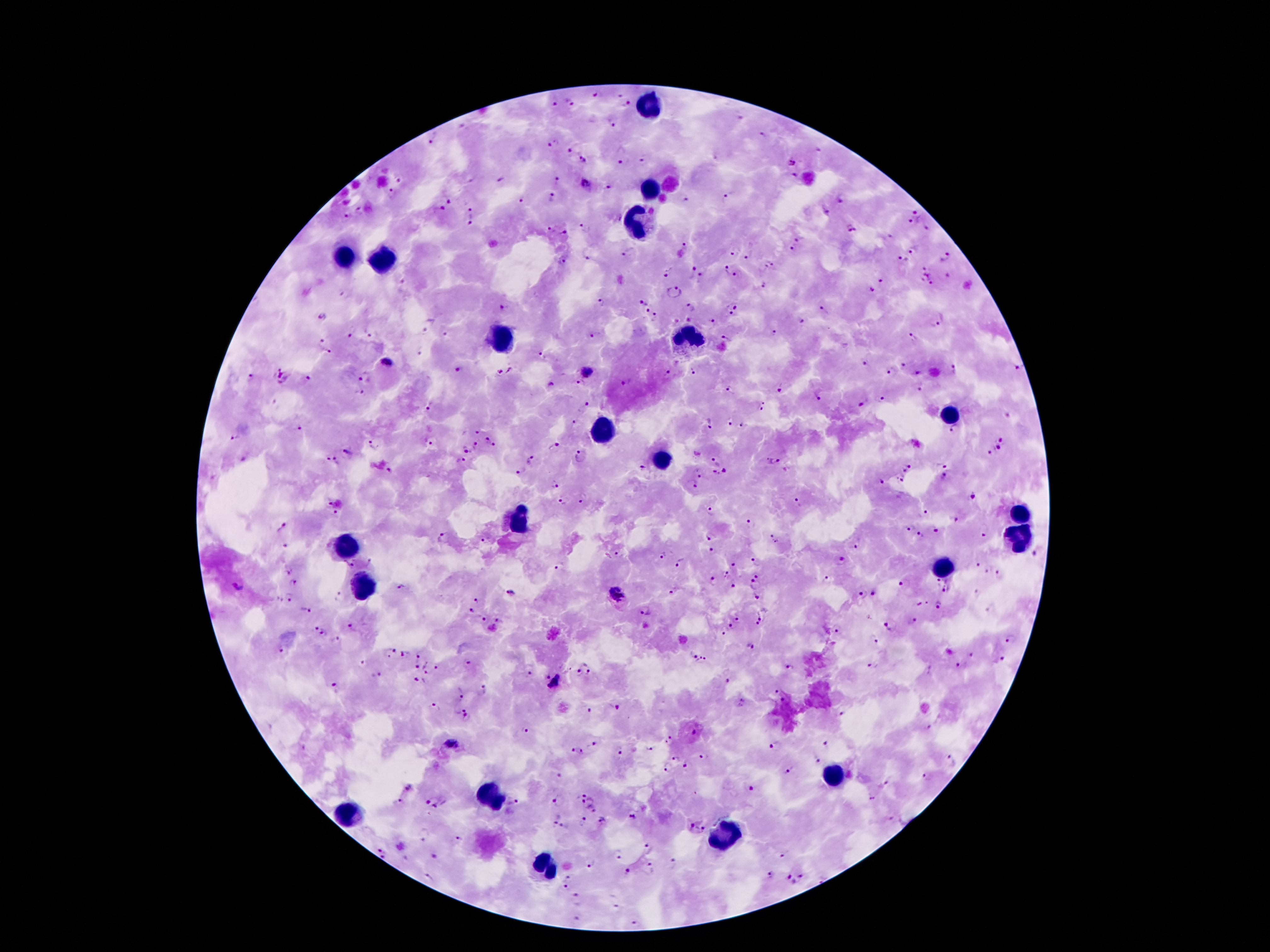
Approximate centers as (x, y) in pixels. Leukocyte locations: (649, 102), (650, 188), (637, 221), (346, 259), (380, 261), (686, 332), (500, 336), (947, 416), (602, 430), (657, 459), (1016, 511), (519, 520), (1018, 541), (348, 547), (941, 566), (364, 586), (830, 775), (489, 797), (346, 814), (725, 836), (546, 866). Malaria parasite locations: (594, 96), (619, 96), (571, 102), (554, 104), (627, 105), (611, 121), (463, 127), (763, 136), (431, 141), (553, 142), (569, 149), (585, 161), (644, 161), (620, 162), (791, 162), (794, 175), (557, 179), (400, 180), (500, 180), (586, 185), (606, 186), (392, 190), (553, 196), (448, 197), (727, 197), (843, 198), (520, 199), (688, 199), (441, 208), (360, 209), (469, 209), (827, 211), (916, 212), (913, 221), (469, 223), (587, 227), (549, 229), (852, 229), (927, 230), (565, 232), (799, 239), (685, 242), (791, 249), (912, 251), (630, 253), (731, 254), (749, 257), (947, 257), (589, 259), (902, 259), (562, 261), (773, 264), (766, 266), (926, 268), (692, 270), (725, 272), (668, 273), (737, 275), (702, 276), (927, 277), (402, 282), (881, 282), (765, 285), (933, 285), (871, 289), (672, 291), (343, 294), (600, 301), (643, 303), (737, 305), (693, 307), (823, 309), (646, 311), (729, 313), (321, 316), (656, 317), (713, 322), (803, 322), (936, 323), (425, 329), (352, 330), (774, 332), (445, 333), (370, 334), (594, 335), (913, 335), (724, 338), (320, 341), (329, 350), (419, 352), (541, 354), (387, 361), (864, 364), (905, 365), (459, 369), (694, 369), (954, 369), (1017, 369), (510, 371), (587, 372), (668, 372), (919, 372), (889, 374), (249, 375), (365, 375), (282, 376), (307, 378), (577, 382), (622, 383), (551, 384), (781, 388), (731, 390), (921, 390), (360, 393), (817, 395), (881, 398), (864, 402), (429, 406), (584, 406), (761, 407), (575, 421), (710, 423), (729, 423), (297, 425), (742, 425), (954, 430), (476, 431), (234, 436), (488, 438), (1003, 438), (431, 441), (916, 443), (474, 444), (494, 444), (373, 445), (554, 447), (465, 448), (997, 449), (346, 452), (989, 453), (578, 456), (329, 459), (715, 459), (462, 460), (531, 460), (774, 460), (337, 461), (942, 464), (644, 467), (909, 467), (389, 470), (521, 470), (725, 470), (904, 471), (716, 474), (944, 475), (699, 476), (882, 480), (899, 480), (554, 483), (690, 485), (972, 496), (582, 497), (560, 502), (329, 503), (799, 503), (711, 509), (927, 512), (336, 513), (956, 518), (750, 522), (282, 528), (908, 529), (936, 531), (920, 535), (710, 536), (442, 537), (774, 537), (984, 537), (482, 539), (858, 543), (286, 544), (712, 549), (615, 555), (1035, 556), (843, 558), (369, 559), (756, 559), (681, 562), (350, 563), (558, 565), (733, 565), (979, 565), (287, 571), (986, 571), (996, 572), (757, 573), (727, 574), (713, 580), (830, 580), (937, 581), (292, 583), (755, 583), (904, 583), (401, 585), (733, 586), (674, 590), (946, 590), (510, 592), (874, 592), (617, 593), (862, 593), (289, 596), (338, 596), (757, 597), (476, 599), (922, 603), (937, 605), (308, 610), (471, 610), (646, 610), (764, 615), (737, 618), (483, 620), (913, 620), (498, 621), (756, 624), (351, 625), (730, 625), (888, 627), (314, 628), (837, 630), (323, 632), (722, 634), (874, 638), (1012, 638), (337, 639), (749, 645), (282, 650), (390, 651), (404, 653), (420, 655), (693, 656), (972, 656), (1003, 659), (702, 660), (360, 662), (469, 663), (874, 665), (416, 666), (425, 666), (958, 666), (436, 667), (789, 667), (427, 671), (578, 671), (588, 672), (529, 674), (378, 675), (548, 676), (416, 679), (726, 680), (556, 682), (335, 687), (485, 690), (775, 691), (462, 693), (783, 700), (435, 706), (618, 707), (461, 708), (591, 710), (843, 714), (467, 719), (929, 726), (523, 731), (693, 732), (670, 740), (594, 742), (827, 743), (451, 744), (776, 745), (572, 748), (651, 748), (582, 751), (618, 753), (702, 755), (676, 758), (816, 759), (951, 761), (686, 765), (668, 767), (789, 770), (559, 773), (927, 777), (885, 784), (408, 785), (752, 788), (585, 795), (871, 799), (399, 800), (560, 800), (515, 801), (582, 801), (435, 802), (590, 806), (595, 811), (632, 815), (555, 819), (603, 820), (584, 822), (691, 826), (565, 828), (702, 830), (426, 833), (460, 839), (400, 846), (646, 846), (381, 849), (435, 856), (619, 856), (782, 856), (384, 857), (406, 858), (673, 861), (650, 865), (591, 866), (627, 871), (770, 874), (428, 876), (788, 876), (802, 876), (569, 878), (794, 882), (566, 886), (577, 899), (617, 905), (576, 917), (635, 923). 100x magnification. Thick peripheral-blood smear. Image is 1270×952 pixels. Giemsa-stained preparation. Smartphone photograph taken through the microscope eyepiece. One field from this slide. Patient malaria status: positive for Plasmodium falciparum.